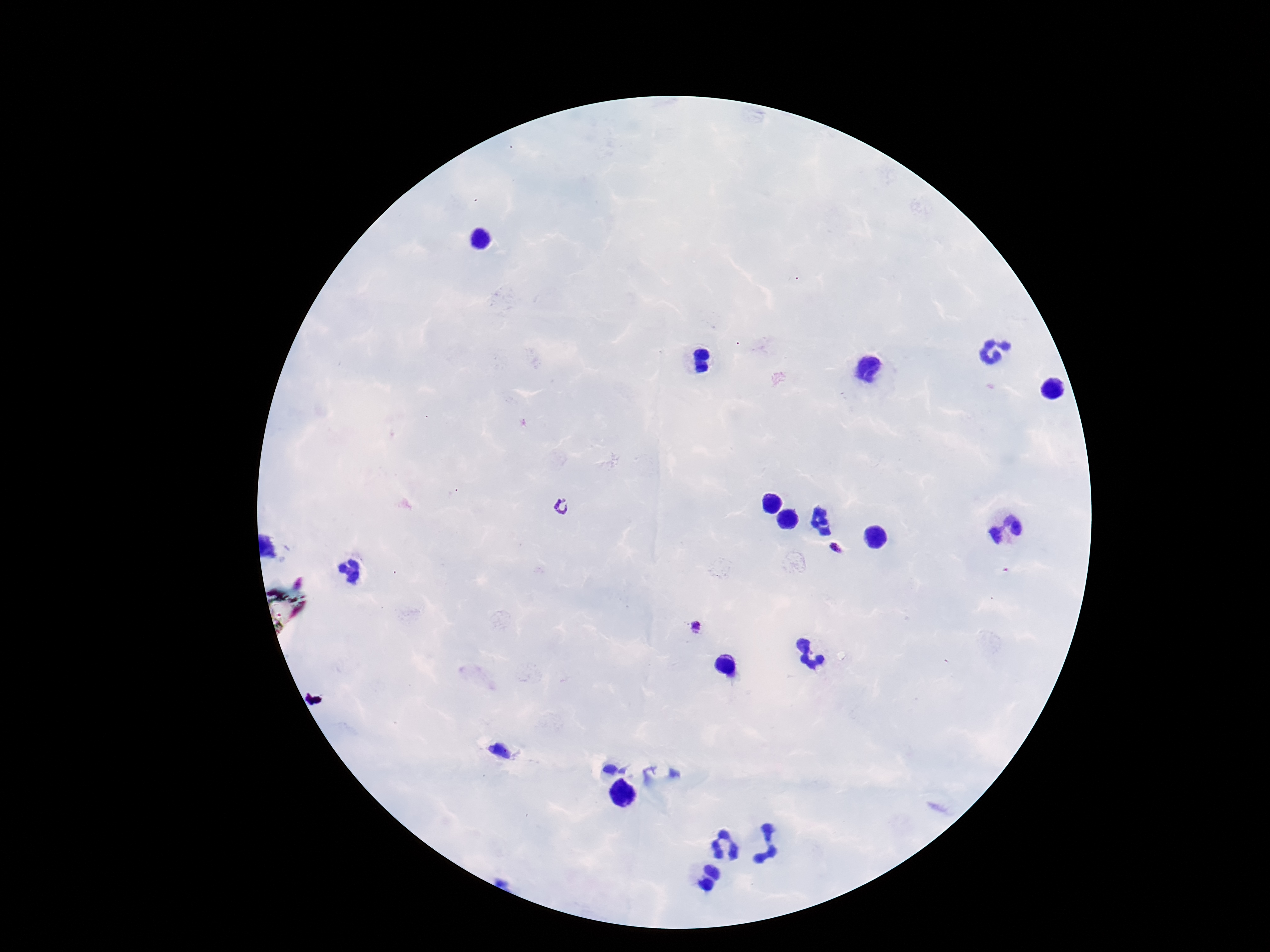

Approximate object centers, in pixels from the top-left corner.
Summary:
  - Plasmodium parasite locations: (x=564, y=506), (x=837, y=548), (x=697, y=627)
  - Capture: smartphone camera through the microscope eyepiece
  - Image size: 1270×952 pixels
  - Patient malaria status: infected
  - Stain: Giemsa
  - Field of view: single
  - Magnification: 100x
  - Preparation: thick blood film